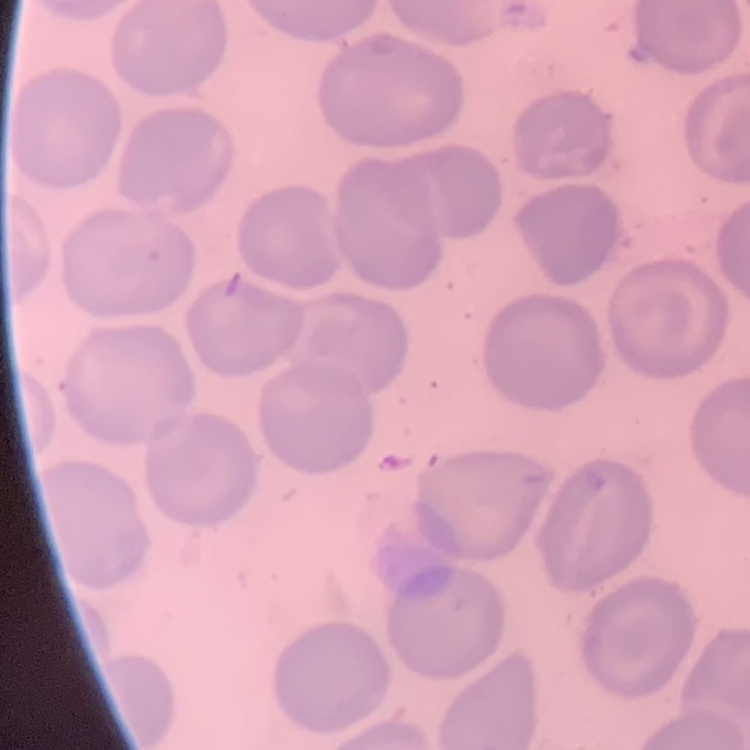
erythrocyte morphology = no rouleaux formation
stain = Field's or Giemsa
preparation = thin blood film
image type = square crop of a larger photomicrograph